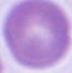

identification = red blood cell
magnification = 1000x
modality = micrograph